Comment on the morphology of the erythrocytes.
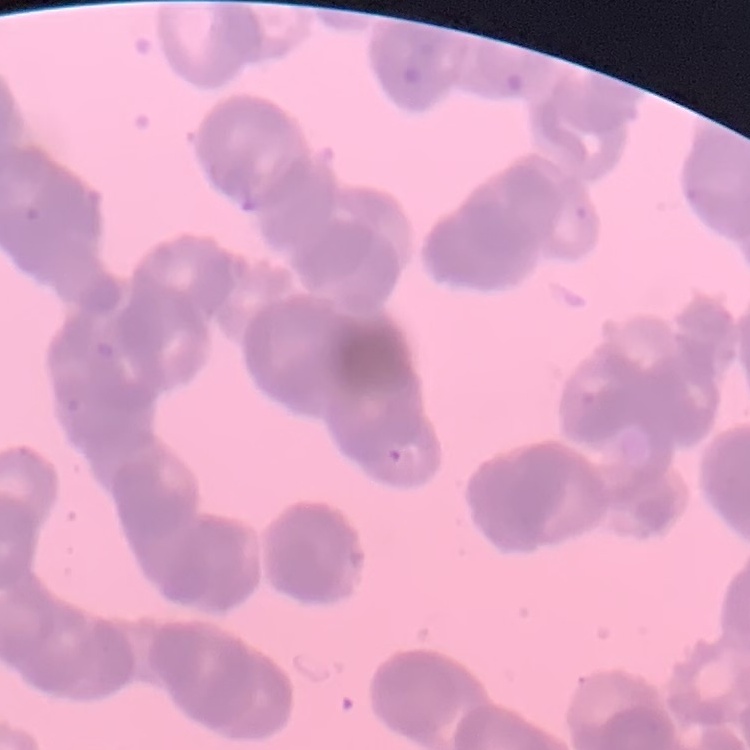

They show rouleaux formation.

Summary:
  - Preparation: thin peripheral smear
  - Stain: Field's or Giemsa
  - Image type: one tile cut from a larger photomicrograph